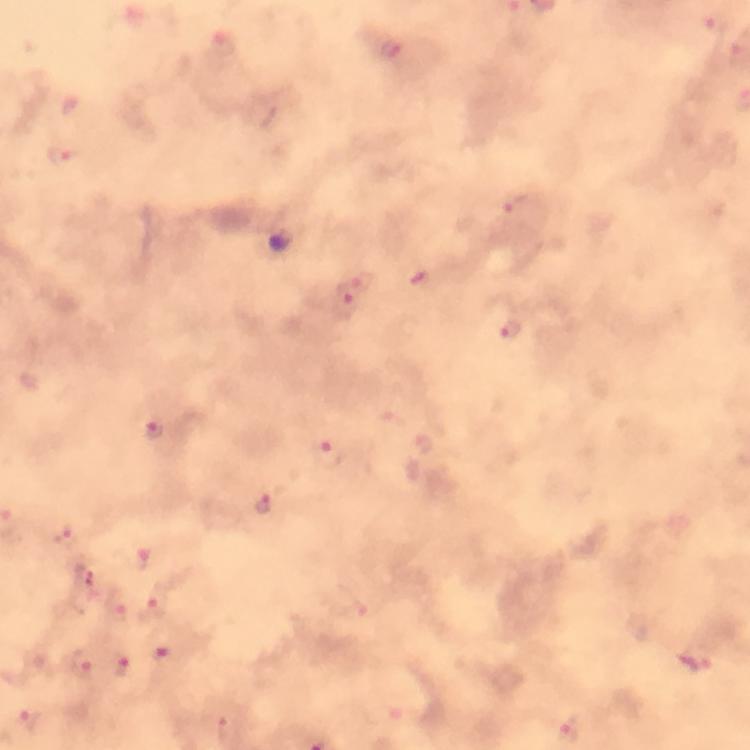

Approximate centers as (x, y) in pixels.
Summary:
  - Plasmodium parasite locations: (717, 26), (394, 51), (67, 154), (516, 205), (364, 282), (346, 303), (511, 334), (154, 431), (330, 456), (265, 505), (68, 534), (86, 580), (155, 605), (167, 658), (698, 663), (80, 664), (121, 666), (29, 718), (570, 732)
  - Preparation: thick blood film
  - Magnification: 100x
  - Image size: 750×750 pixels
  - Immersion oil: applied
  - Stain: Giemsa
  - Capture: smartphone photograph through a microscope
  - Cropped from: a single field of view
  - Context: from a malaria diagnostic workup